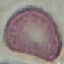

Summary:
  - Result: no malaria parasites seen
  - Capture: smartphone camera at the microscope eyepiece
  - Image type: cell patch, automatically extracted from a larger field of view and resized to 64 × 64 pixels
  - Stain: Giemsa
  - Preparation: thin blood smear